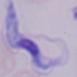
Summary:
  - Modality: photomicrograph
  - Identification: trypanosome
  - Magnification: 1000x